Outline each blood parasite and name the species.
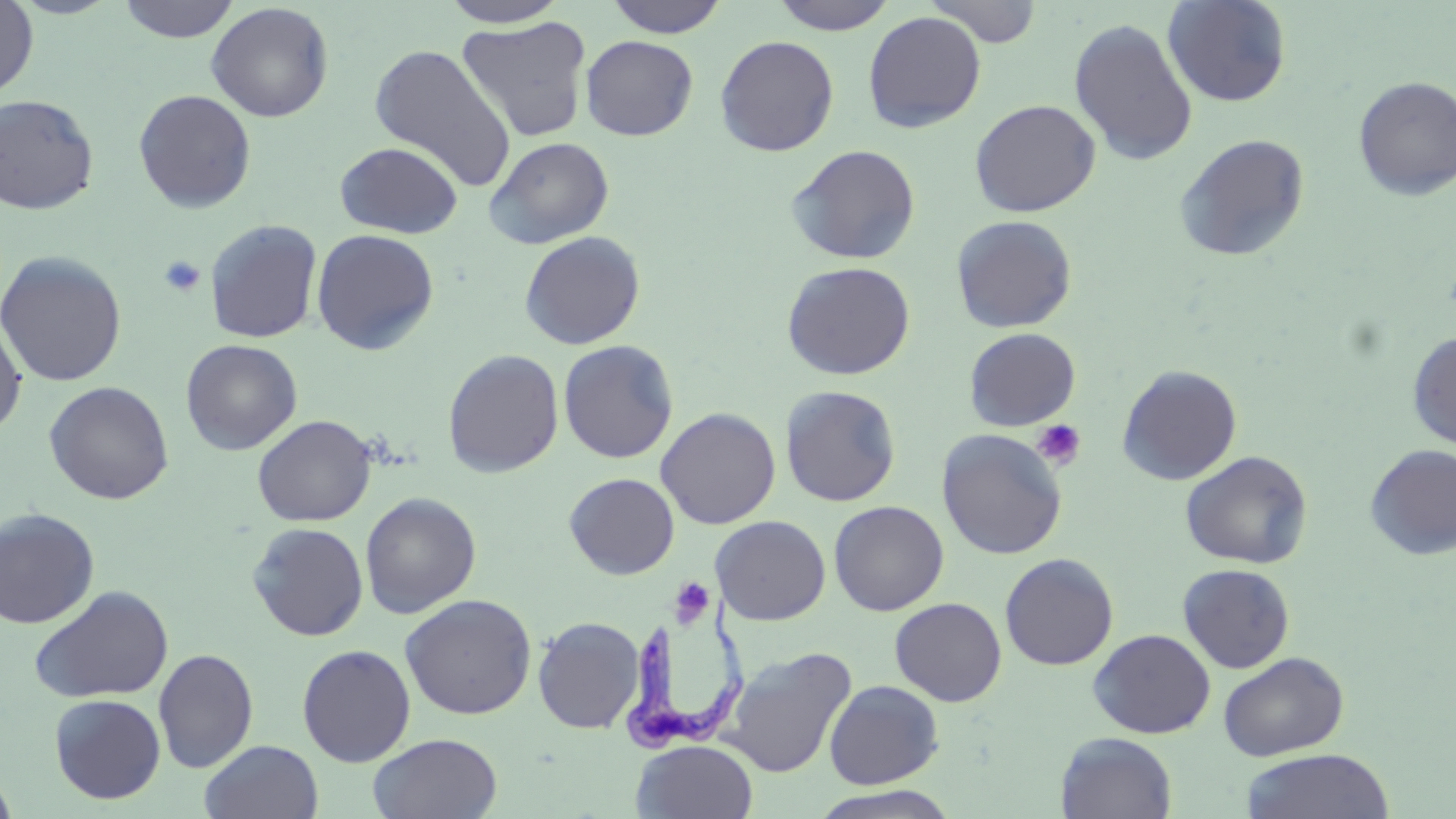

Approximate bounding boxes as (x1,y1)-(x2,y2) corner pairs in pixels.
Trypanosoma brucei: (617,592)-(750,755).
No Plasmodium falciparum, Plasmodium ovale, Plasmodium malariae, Plasmodium vivax, or Babesia divergens observed.

Summary:
  - Uninfected red blood cell locations: (0,0)-(38,99), (8,0)-(124,19), (117,0)-(240,43), (606,0)-(729,38), (769,0)-(899,35), (926,0)-(1044,48), (1162,0)-(1292,107), (439,1)-(571,28), (206,3)-(334,122), (862,11)-(986,133), (455,16)-(592,143), (1068,17)-(1198,166), (580,35)-(699,140), (715,35)-(839,156), (369,43)-(516,190), (1353,76)-(1456,201), (133,89)-(257,213), (0,94)-(99,215), (969,99)-(1101,217), (1174,134)-(1311,263), (485,136)-(614,249), (334,141)-(464,238), (786,144)-(921,264), (950,215)-(1077,333), (204,219)-(323,343), (311,228)-(439,355), (519,231)-(645,350), (0,251)-(126,387), (781,260)-(916,380), (0,316)-(27,436), (963,327)-(1081,431), (1407,331)-(1456,450), (180,339)-(302,455), (558,340)-(679,463), (443,349)-(564,477), (1116,364)-(1242,485), (44,381)-(174,505), (780,385)-(901,507), (655,407)-(781,529), (253,414)-(376,526), (937,429)-(1067,560), (1364,443)-(1456,560), (1180,451)-(1312,569), (564,473)-(680,579), (360,492)-(481,618), (828,500)-(949,616), (0,508)-(100,628), (711,515)-(830,624), (247,521)-(369,641), (999,552)-(1118,670), (1177,563)-(1295,673), (29,585)-(174,704), (399,593)-(537,720), (889,597)-(1007,707), (533,616)-(645,734), (1088,628)-(1215,739), (297,644)-(416,766), (721,646)-(857,779), (153,648)-(258,773), (1218,651)-(1349,761), (823,679)-(944,789), (48,694)-(166,804), (368,732)-(503,818), (1055,732)-(1178,818), (199,739)-(324,819), (631,739)-(759,819), (1240,748)-(1394,819), (0,768)-(18,819), (809,784)-(963,819)
  - Platelet locations: (158,255)-(206,297), (1031,419)-(1086,470), (673,581)-(712,625)
  - Slide-level diagnosis: Trypanosoma brucei
  - Magnification: 1000x
  - Preparation: thin blood smear
  - Field of view: single
  - Image size: 1456×819 pixels
  - Stain: May-Grünwald-Giemsa
  - Modality: optical microscopy